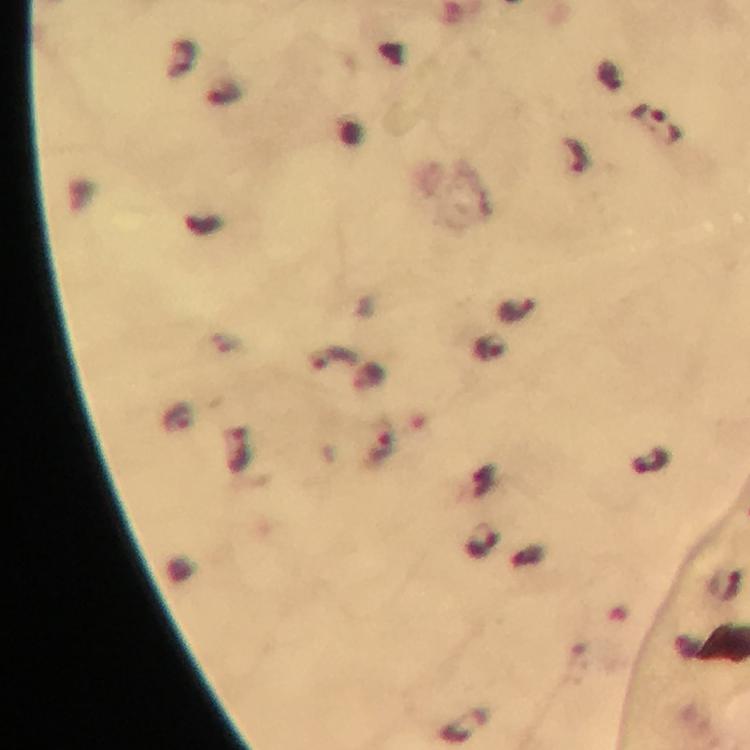

{
  "plasmodium_parasite_locations": "approximate centers as [x, y] in pixels: [657, 124], [576, 155], [516, 310], [489, 350], [336, 358], [381, 442], [483, 542]",
  "context": "from a diagnostic examination for malaria",
  "image_size": "750×750 pixels",
  "stain": "Giemsa",
  "immersion_oil": "applied",
  "cropped_from": "one field of view",
  "capture": "smartphone mounted on the microscope",
  "preparation": "thick blood film",
  "magnification": "100x"
}